Classify this cell by malaria status.
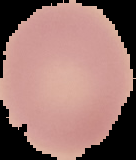

Uninfected.

Summary:
  - Image size: 136×160 pixels
  - Image type: segmented cell region with the area outside set to black
  - Preparation: thin blood film